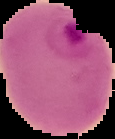

Summary:
  - Image size: 115×139 pixels
  - Image type: segmented cell region on a black background
  - Preparation: thin blood film
  - Malaria status: parasitized